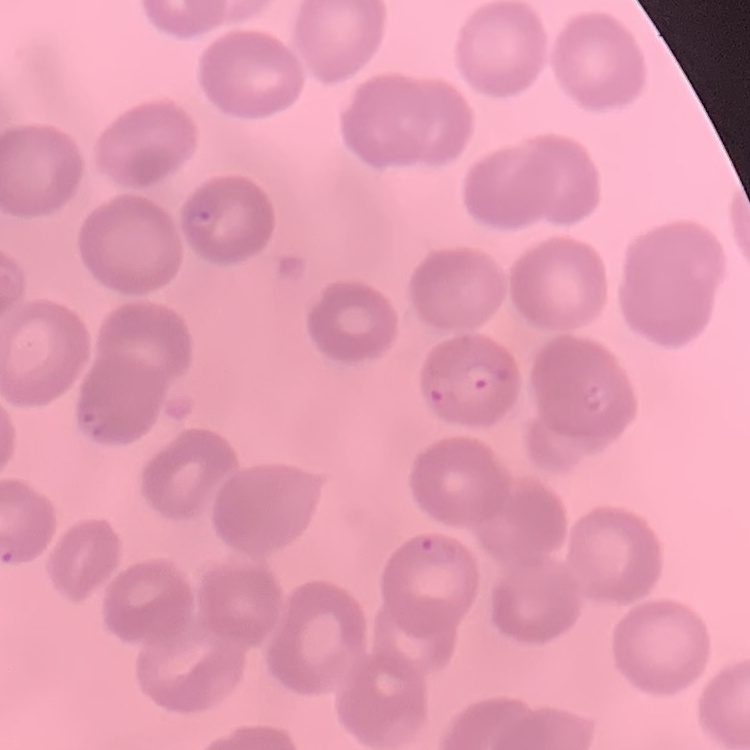 The red blood cells show no rouleaux formation. Field's or Giemsa stain. Square crop of a larger photomicrograph. Thin blood smear.